Outline each uninfected red blood cell.
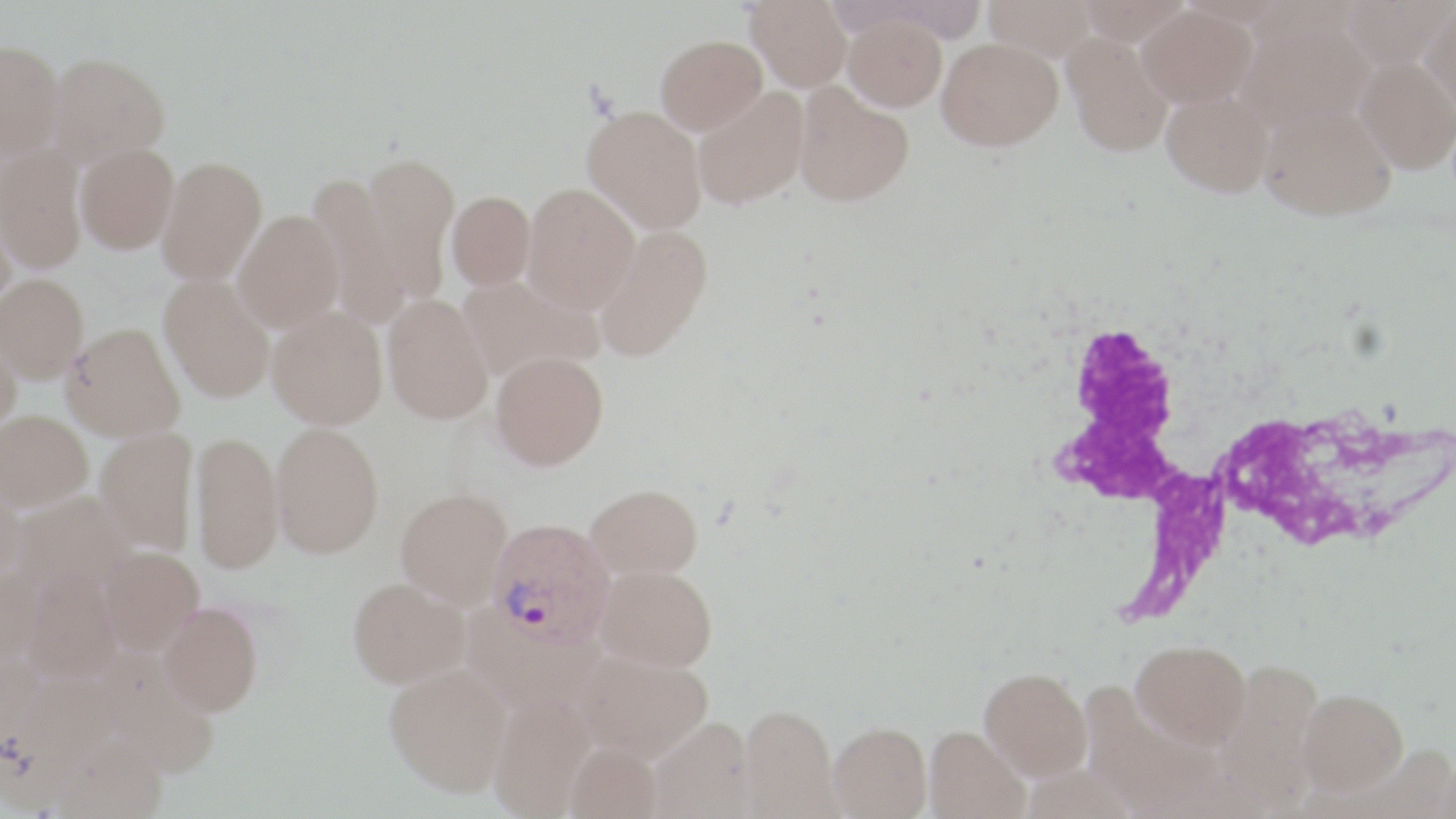
Approximate bounding boxes as named x1/y1/x2/y2 corners in pixels.
Uninfected red blood cells: (x1=746, y1=0, x2=852, y2=90), (x1=983, y1=0, x2=1098, y2=61), (x1=1076, y1=0, x2=1192, y2=47), (x1=1341, y1=0, x2=1453, y2=71), (x1=1421, y1=2, x2=1456, y2=119), (x1=1138, y1=6, x2=1257, y2=110), (x1=842, y1=13, x2=946, y2=111), (x1=1235, y1=13, x2=1373, y2=138), (x1=1062, y1=33, x2=1172, y2=160), (x1=656, y1=34, x2=766, y2=134), (x1=0, y1=39, x2=64, y2=158), (x1=936, y1=39, x2=1062, y2=155), (x1=48, y1=52, x2=170, y2=167), (x1=1355, y1=57, x2=1456, y2=175), (x1=793, y1=82, x2=914, y2=207), (x1=693, y1=87, x2=809, y2=209), (x1=1162, y1=94, x2=1273, y2=200), (x1=582, y1=104, x2=706, y2=233), (x1=1259, y1=104, x2=1395, y2=223), (x1=75, y1=142, x2=178, y2=254), (x1=0, y1=146, x2=87, y2=273), (x1=361, y1=152, x2=458, y2=302), (x1=157, y1=156, x2=267, y2=285), (x1=307, y1=174, x2=409, y2=329), (x1=523, y1=183, x2=640, y2=313), (x1=446, y1=191, x2=535, y2=290), (x1=0, y1=196, x2=16, y2=311), (x1=233, y1=210, x2=345, y2=332), (x1=593, y1=224, x2=714, y2=362), (x1=0, y1=273, x2=89, y2=382), (x1=159, y1=275, x2=275, y2=403), (x1=458, y1=275, x2=603, y2=382), (x1=382, y1=294, x2=493, y2=424), (x1=267, y1=306, x2=388, y2=428), (x1=63, y1=322, x2=186, y2=441), (x1=0, y1=330, x2=22, y2=436), (x1=490, y1=350, x2=609, y2=469), (x1=0, y1=410, x2=93, y2=510), (x1=271, y1=422, x2=384, y2=557), (x1=95, y1=428, x2=198, y2=554), (x1=191, y1=430, x2=282, y2=573), (x1=0, y1=471, x2=25, y2=579), (x1=586, y1=483, x2=703, y2=579), (x1=395, y1=488, x2=513, y2=609), (x1=10, y1=491, x2=133, y2=596), (x1=100, y1=546, x2=204, y2=654), (x1=596, y1=564, x2=717, y2=671), (x1=0, y1=566, x2=42, y2=672), (x1=22, y1=569, x2=122, y2=685), (x1=348, y1=577, x2=469, y2=687), (x1=159, y1=601, x2=262, y2=715), (x1=1132, y1=639, x2=1251, y2=747), (x1=93, y1=648, x2=220, y2=778), (x1=577, y1=649, x2=713, y2=761), (x1=1214, y1=658, x2=1325, y2=804), (x1=384, y1=662, x2=512, y2=796), (x1=979, y1=667, x2=1092, y2=779), (x1=1297, y1=688, x2=1408, y2=795), (x1=489, y1=695, x2=594, y2=818), (x1=738, y1=704, x2=839, y2=816), (x1=650, y1=717, x2=755, y2=819), (x1=829, y1=722, x2=932, y2=818), (x1=924, y1=726, x2=1029, y2=819), (x1=55, y1=733, x2=166, y2=818), (x1=565, y1=741, x2=662, y2=819).

Summary:
  - White blood cell locations: (x1=1044, y1=311, x2=1321, y2=628)
  - Plasmodium vivax-infected red blood cell locations: (x1=486, y1=517, x2=617, y2=650)
  - Slide-level diagnosis: Plasmodium vivax
  - Stain: May-Grünwald-Giemsa
  - Image size: 1456×819 pixels
  - Field of view: one of a larger specimen
  - Magnification: 1000x
  - Modality: optical microscopy
  - Preparation: thin blood film